Report the malaria status of this cell.
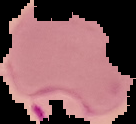

Parasitized.

image size = 136×124 pixels
image type = cell region segmented out of the field of view; surrounding area masked to black
preparation = thin blood smear